Classify this cell by malaria status.
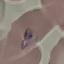
It is parasitized.

image type = automatically extracted cell patch, resized to 64 × 64 pixels
preparation = thin blood film
capture = smartphone camera at the microscope eyepiece
stain = Giemsa